Describe the morphology of the red blood cells.
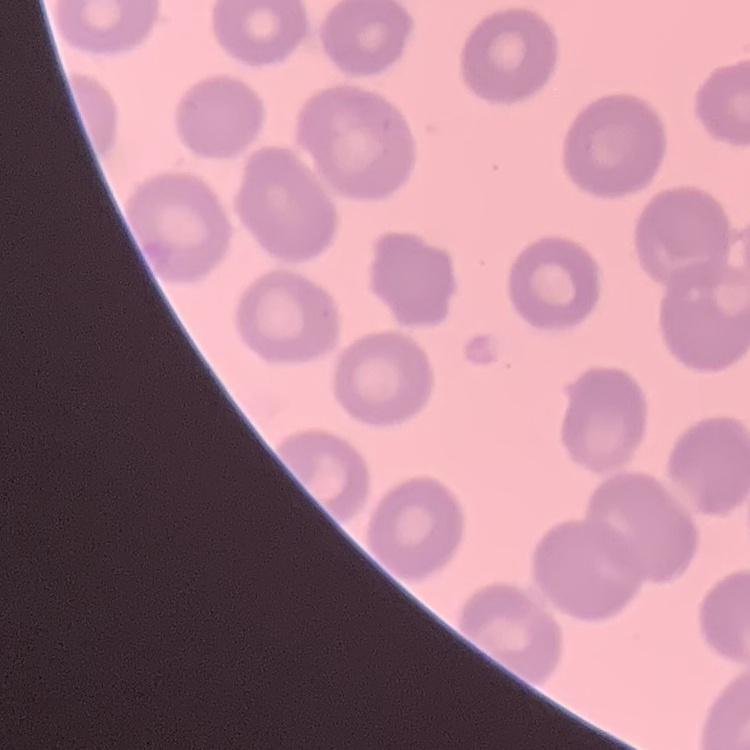

They show no rouleaux formation.

Thin blood film. Field's or Giemsa stain. One tile cut from a larger photomicrograph.